Point out each malaria parasite.
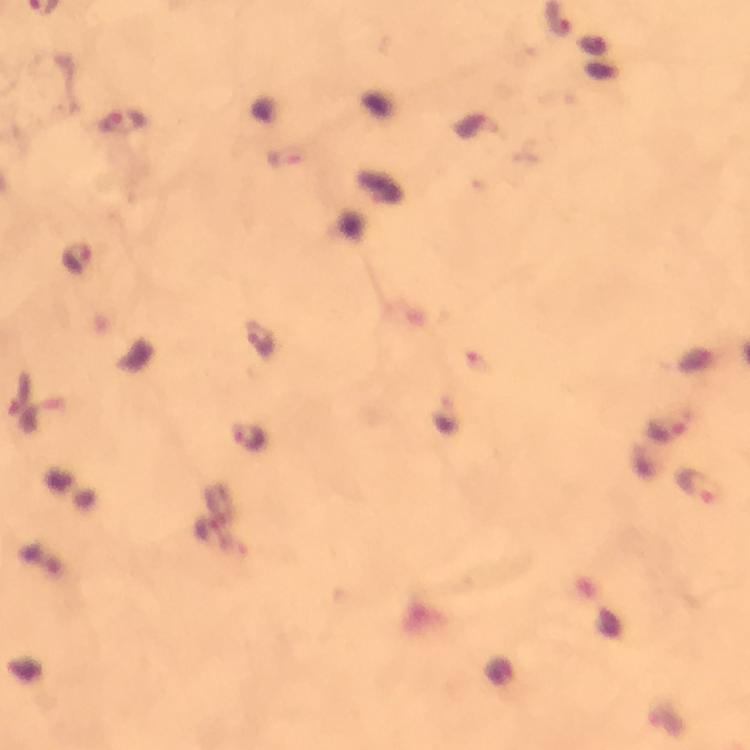

Approximate centers as {x, y} in pixels.
Malaria parasites: {123, 122}, {77, 257}, {259, 340}, {665, 429}, {248, 436}, {699, 485}.

Immersion oil was used. Giemsa-stained preparation. 100x magnification. Photographed through the microscope with a smartphone camera. Thick smear. Image is 750×750 pixels. A crop from one field of view. From a diagnostic examination for malaria.